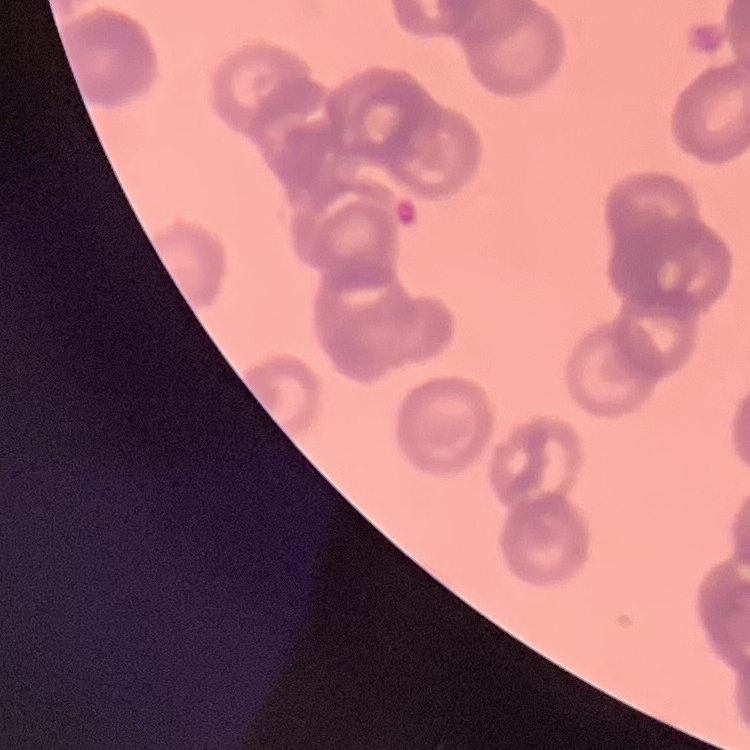
The erythrocytes show rouleaux formation. One tile cut from a larger photomicrograph. Stained with either Field's or Giemsa. Thin blood film.